Classify this cell by malaria status.
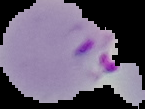
It is parasitized.

From a thin blood smear. Cell region segmented out of the field of view; the surrounding area is masked to black. Image is 145×109 pixels.